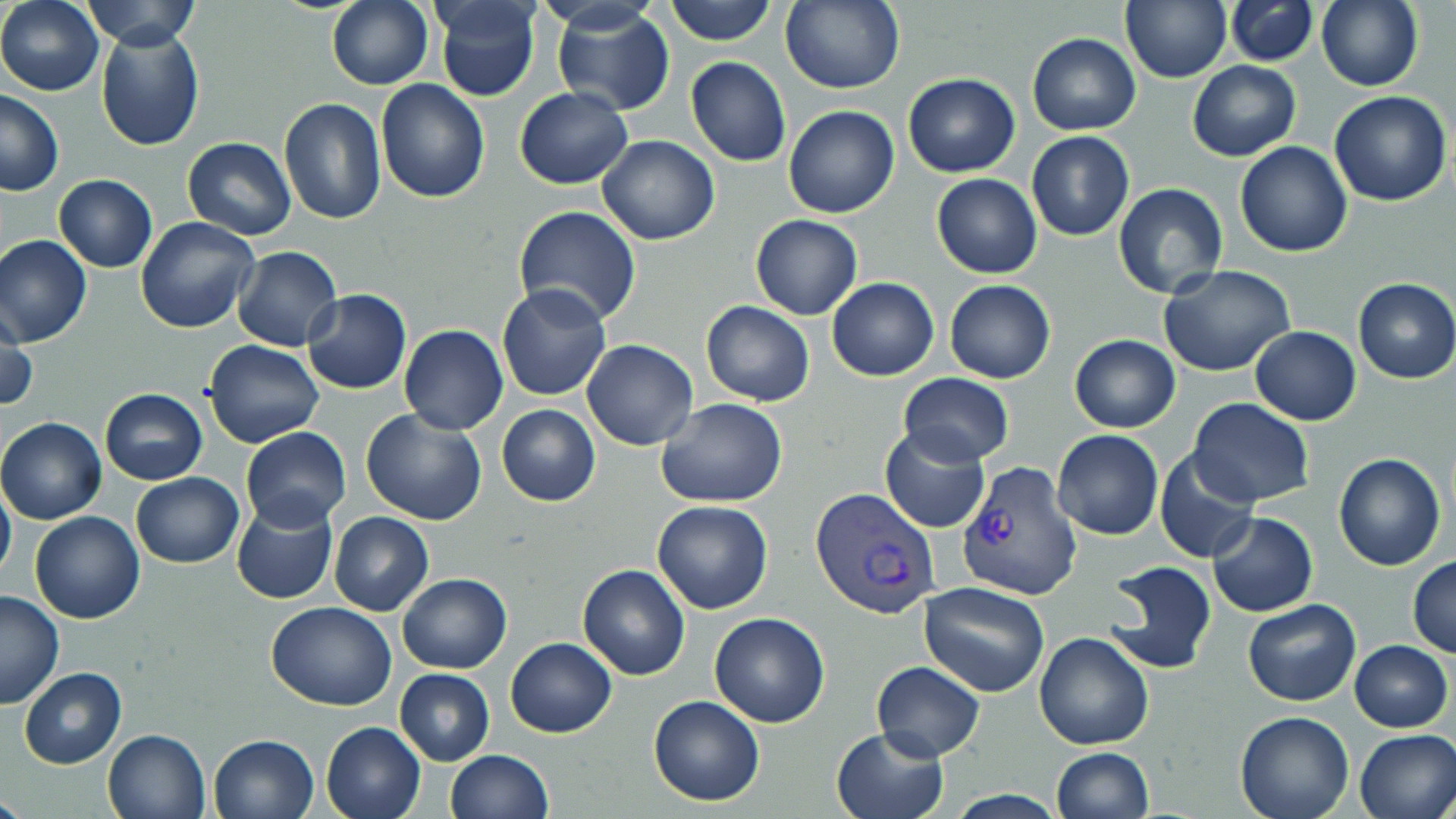

slide_level_diagnosis: Plasmodium vivax
preparation: thin blood smear
modality: light microscopy
stain: May-Grünwald-Giemsa
uninfected_red_blood_cell_locations: 'approximate bounding boxes as named x1/y1/x2/y2 corners in pixels: (x1=1, y1=0, x2=103, y2=95), (x1=431, y1=0, x2=543, y2=103), (x1=665, y1=0, x2=777, y2=46), (x1=1121, y1=0, x2=1232, y2=85), (x1=82, y1=1, x2=198, y2=49), (x1=326, y1=1, x2=433, y2=89), (x1=782, y1=1, x2=906, y2=95), (x1=1224, y1=1, x2=1319, y2=66), (x1=1316, y1=1, x2=1422, y2=91), (x1=551, y1=5, x2=676, y2=116), (x1=96, y1=25, x2=205, y2=151), (x1=1028, y1=33, x2=1141, y2=136), (x1=686, y1=57, x2=790, y2=167), (x1=1187, y1=60, x2=1300, y2=161), (x1=902, y1=72, x2=1020, y2=177), (x1=375, y1=80, x2=490, y2=203), (x1=515, y1=87, x2=633, y2=188), (x1=1, y1=90, x2=64, y2=195), (x1=1328, y1=90, x2=1453, y2=207), (x1=279, y1=97, x2=387, y2=225), (x1=784, y1=104, x2=900, y2=219), (x1=1026, y1=132, x2=1134, y2=241), (x1=596, y1=134, x2=720, y2=245), (x1=181, y1=137, x2=297, y2=240), (x1=1235, y1=141, x2=1353, y2=257), (x1=54, y1=174, x2=158, y2=271), (x1=932, y1=174, x2=1042, y2=279), (x1=1112, y1=182, x2=1228, y2=299), (x1=512, y1=206, x2=641, y2=329), (x1=750, y1=214, x2=862, y2=321), (x1=135, y1=218, x2=261, y2=333), (x1=0, y1=234, x2=93, y2=347), (x1=232, y1=246, x2=342, y2=351), (x1=1157, y1=265, x2=1298, y2=379), (x1=826, y1=277, x2=939, y2=381), (x1=1352, y1=278, x2=1456, y2=384), (x1=943, y1=279, x2=1056, y2=384), (x1=497, y1=283, x2=612, y2=401), (x1=301, y1=289, x2=412, y2=394), (x1=700, y1=300, x2=815, y2=407), (x1=1, y1=312, x2=36, y2=415), (x1=399, y1=324, x2=508, y2=435), (x1=1250, y1=327, x2=1361, y2=426), (x1=1069, y1=335, x2=1180, y2=434), (x1=581, y1=339, x2=698, y2=451), (x1=204, y1=341, x2=324, y2=448), (x1=897, y1=372, x2=1015, y2=466), (x1=100, y1=388, x2=207, y2=485), (x1=655, y1=397, x2=787, y2=506), (x1=1187, y1=398, x2=1313, y2=508), (x1=496, y1=404, x2=600, y2=506), (x1=360, y1=410, x2=489, y2=527), (x1=1, y1=417, x2=107, y2=524), (x1=240, y1=427, x2=351, y2=531), (x1=879, y1=428, x2=990, y2=534), (x1=1052, y1=429, x2=1163, y2=540), (x1=1155, y1=450, x2=1260, y2=564), (x1=1333, y1=453, x2=1446, y2=571), (x1=131, y1=473, x2=243, y2=568), (x1=0, y1=477, x2=15, y2=587), (x1=651, y1=500, x2=774, y2=613), (x1=231, y1=501, x2=337, y2=605), (x1=29, y1=511, x2=145, y2=623), (x1=329, y1=511, x2=434, y2=615), (x1=1207, y1=512, x2=1317, y2=617), (x1=1407, y1=556, x2=1456, y2=656), (x1=1103, y1=560, x2=1216, y2=676), (x1=577, y1=564, x2=690, y2=681), (x1=396, y1=573, x2=511, y2=674), (x1=919, y1=582, x2=1051, y2=696), (x1=0, y1=592, x2=64, y2=710), (x1=1242, y1=599, x2=1361, y2=707), (x1=266, y1=602, x2=397, y2=710), (x1=709, y1=611, x2=831, y2=728), (x1=1035, y1=632, x2=1154, y2=750), (x1=505, y1=637, x2=617, y2=738), (x1=1350, y1=640, x2=1453, y2=733), (x1=871, y1=661, x2=986, y2=761), (x1=20, y1=668, x2=127, y2=768), (x1=394, y1=668, x2=494, y2=766), (x1=647, y1=695, x2=765, y2=805), (x1=1235, y1=711, x2=1356, y2=819), (x1=320, y1=720, x2=427, y2=819), (x1=831, y1=726, x2=948, y2=819), (x1=103, y1=728, x2=212, y2=819), (x1=1353, y1=728, x2=1456, y2=819), (x1=208, y1=733, x2=320, y2=819), (x1=1050, y1=747, x2=1154, y2=819), (x1=444, y1=750, x2=553, y2=819)'
magnification: 1000x
field_of_view: one of a larger specimen
image_size: 1456×819 pixels
plasmodium_vivax_infected_red_blood_cell_locations: 'approximate bounding boxes as named x1/y1/x2/y2 corners in pixels: (x1=956, y1=459, x2=1079, y2=599), (x1=809, y1=485, x2=941, y2=620)'